Assess for malaria.
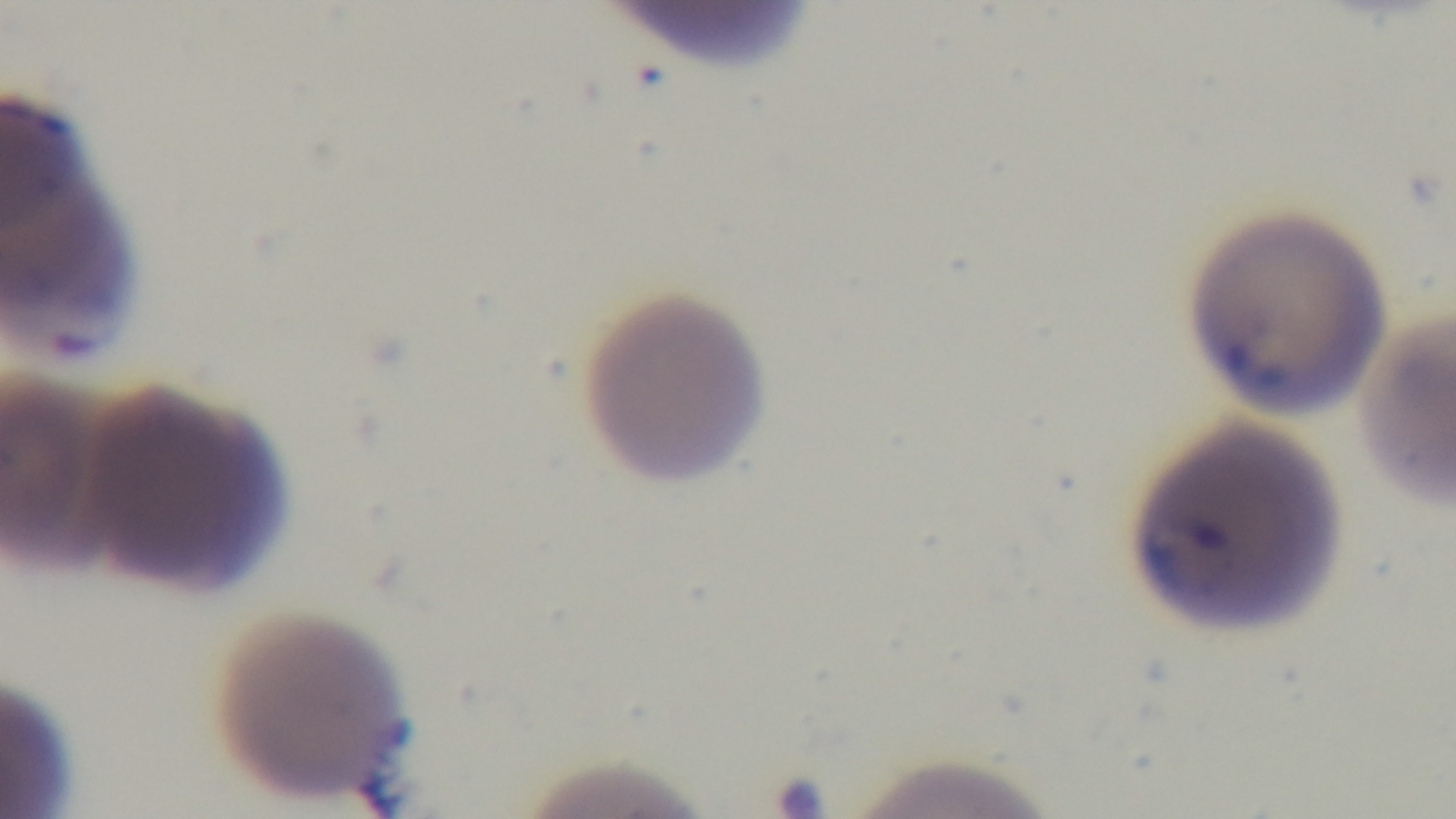

Infected.

Preparation: thin blood film. Single field of view. Light microscopy. Oil-immersion objective, 100x. Giemsa stain. Mounted 4K digital camera.